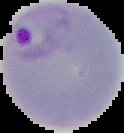

Summary:
  - Image size: 124×133 pixels
  - Preparation: thin blood film
  - Malaria status: parasitized
  - Image type: segmented cell region on a black background